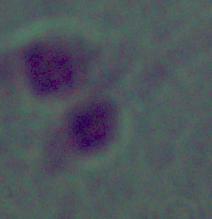
Photomicrograph. A Leishmania parasite is shown. Captured at 1000x magnification.